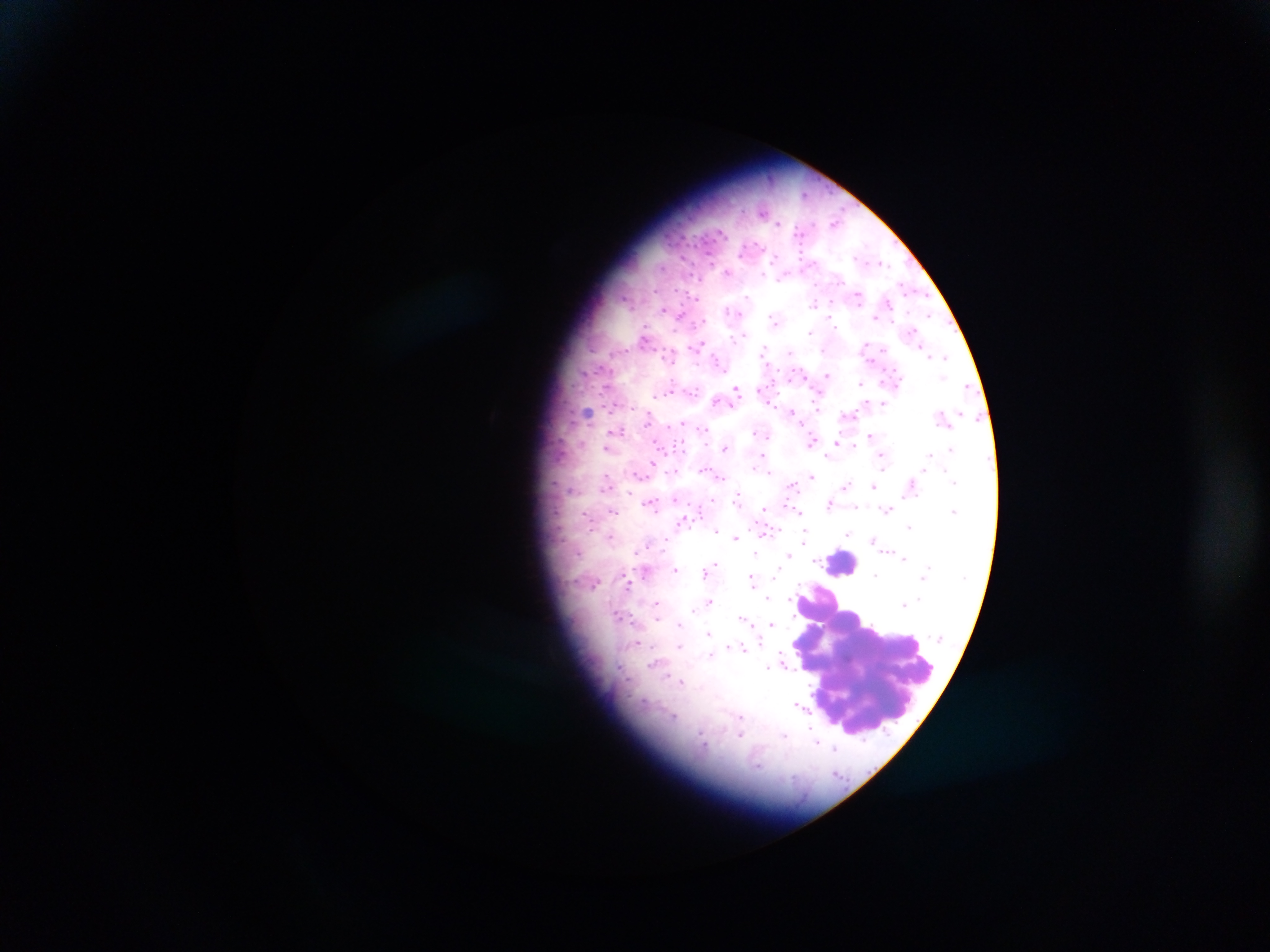

{
  "field_of_view": "single",
  "country": "Ghana",
  "capture": "mobile-phone photograph through a microscope",
  "preparation": "thick blood film",
  "leukocyte_locations": "approximate centers as [x, y] in pixels: [843, 563], [868, 656]",
  "image_size": "1270×952 pixels",
  "malaria_parasite_locations": "approximate centers as [x, y] in pixels: [784, 224], [718, 237], [701, 252], [800, 256], [762, 269], [691, 274], [907, 290], [813, 305], [663, 309], [729, 309], [772, 318], [929, 318], [698, 321], [734, 336], [699, 344], [764, 346], [612, 354], [867, 354], [946, 357], [667, 363], [827, 375], [943, 377], [770, 378], [600, 380], [861, 383], [966, 386], [736, 388], [669, 392], [588, 410], [790, 411], [849, 414], [942, 415], [643, 425], [682, 427], [704, 431], [870, 435], [812, 438], [836, 441], [724, 447], [606, 448], [950, 448], [763, 454], [927, 455], [885, 459], [653, 462], [675, 470], [721, 476], [812, 476], [607, 479], [951, 479], [954, 480], [846, 483], [791, 486], [874, 486], [650, 501], [830, 503], [736, 504], [887, 510], [954, 510], [798, 511], [614, 512], [686, 516], [908, 526], [716, 528], [773, 529], [805, 534], [846, 535], [734, 536], [805, 539], [872, 541], [665, 543], [756, 550], [789, 555], [905, 559], [817, 560], [711, 564], [676, 568], [704, 570], [876, 574], [752, 578], [596, 583], [629, 586], [766, 599], [710, 600], [791, 600], [655, 604], [901, 604], [695, 606], [692, 611], [618, 614], [742, 619], [657, 621], [679, 624], [772, 624], [708, 632], [758, 642], [638, 643], [680, 646], [742, 648], [711, 655], [783, 664], [766, 667], [678, 680], [798, 703], [672, 716], [741, 734], [783, 735], [702, 738], [817, 741], [834, 749], [836, 773]"
}